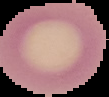 Segmented cell region on a black background. From a thin blood smear. Malaria status: uninfected. Image is 109×97 pixels.